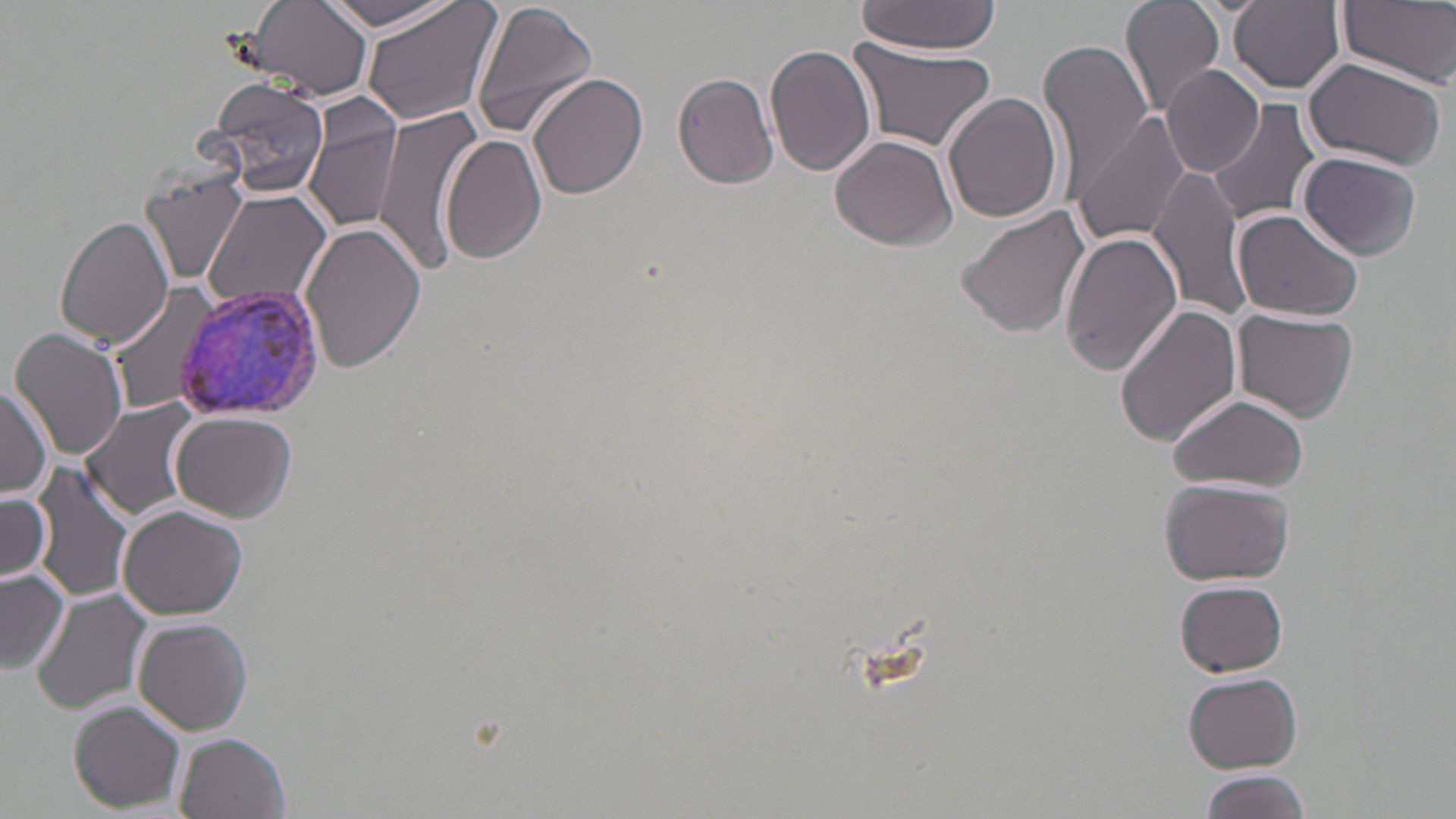
Approximate bounding boxes as (x1, y1, x2, y2) in pixels. Plasmodium vivax-infected red blood cell locations: (172, 283, 328, 424). Uninfected red blood cell locations: (361, 0, 502, 127), (471, 0, 598, 140), (1119, 0, 1228, 118), (1229, 0, 1346, 92), (1339, 0, 1456, 88), (238, 1, 376, 102), (317, 1, 465, 34), (857, 1, 998, 55), (848, 37, 999, 155), (1040, 38, 1154, 187), (768, 45, 878, 177), (1301, 56, 1447, 168), (1162, 65, 1265, 178), (673, 73, 779, 189), (527, 74, 648, 201), (205, 79, 331, 199), (943, 92, 1064, 223), (1206, 100, 1320, 227), (373, 106, 480, 275), (304, 107, 405, 234), (1072, 112, 1193, 246), (442, 132, 549, 266), (831, 135, 958, 250), (1298, 151, 1421, 260), (1150, 164, 1252, 321), (141, 175, 251, 287), (201, 189, 333, 314), (956, 206, 1089, 338), (1233, 209, 1363, 320), (56, 215, 174, 347), (299, 222, 426, 373), (1060, 230, 1183, 374), (108, 285, 222, 416), (1116, 303, 1243, 447), (1235, 309, 1358, 420), (10, 329, 129, 463), (0, 382, 51, 501), (1167, 392, 1308, 493), (80, 398, 202, 520), (172, 412, 295, 521), (31, 460, 137, 606), (1161, 476, 1296, 585), (0, 489, 54, 586), (117, 505, 248, 620), (0, 567, 71, 673), (1176, 578, 1288, 676), (30, 587, 152, 716), (132, 617, 252, 734), (1184, 672, 1304, 772), (70, 700, 186, 812), (173, 732, 290, 819), (1198, 769, 1309, 819). Slide-level diagnosis: Plasmodium vivax. Image is 1456×819 pixels. Thin blood smear. May-Grünwald-Giemsa-stained preparation. Single field of view. Optical microscopy. 1000x magnification.